Assess this cell for malaria.
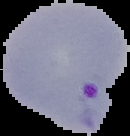

Parasitized.

Cell region segmented out of the field of view; the surrounding area is masked to black. Image is 130×136 pixels. From a thin blood film.